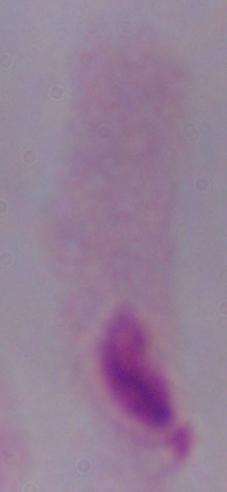
identification: trichomonad
modality: photomicrograph
magnification: 1000x